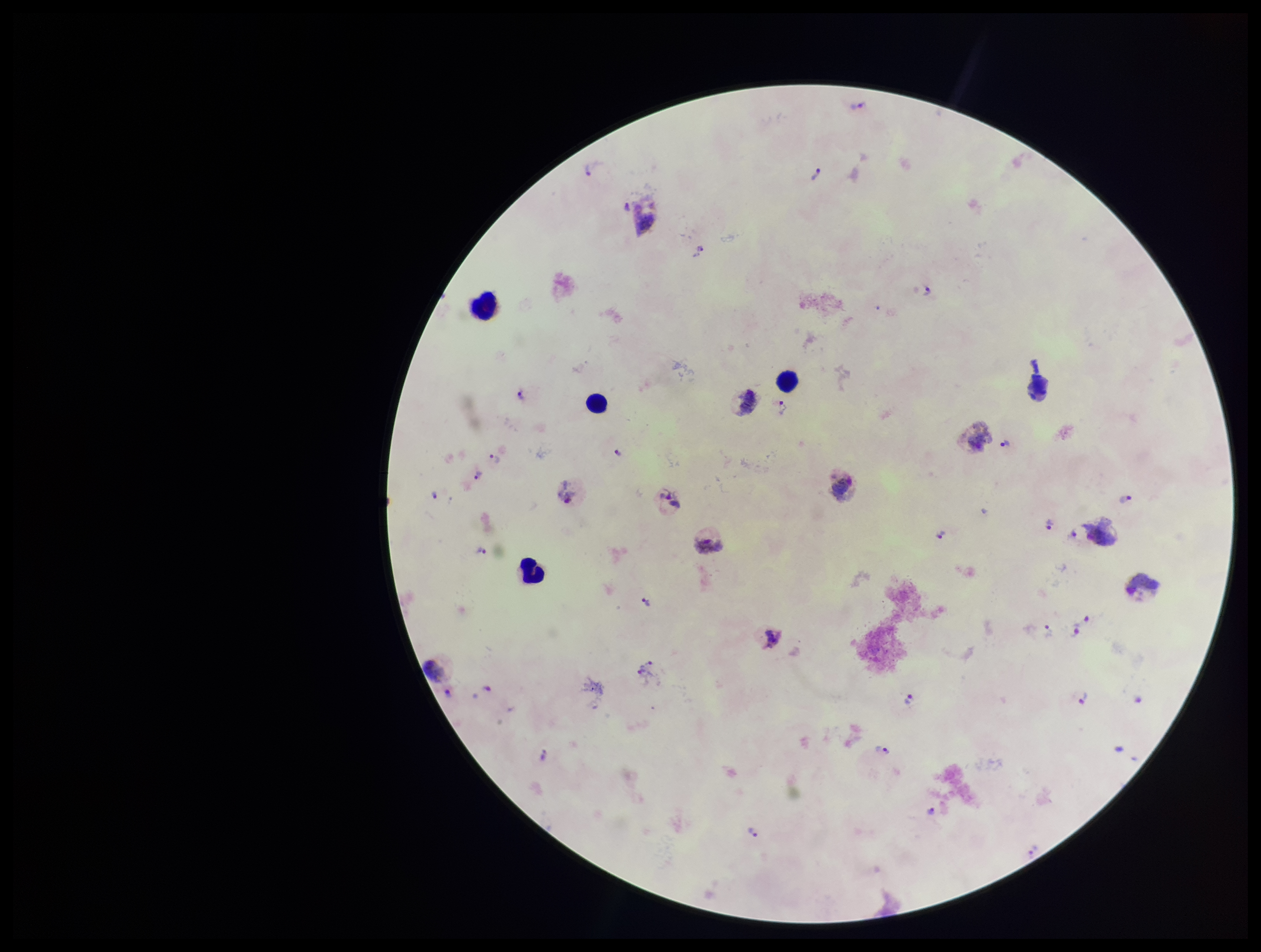
Plasmodium parasites: detected. Species reported for this patient: Plasmodium vivax. One field from this slide. Parasite count: 29. Patient malaria status: positive. Preparation: thick. Leukocyte count: 4. Photographed through the microscope eyepiece with a smartphone camera. Giemsa stain. Image is 1261×952 pixels.